Name the parasite shown.
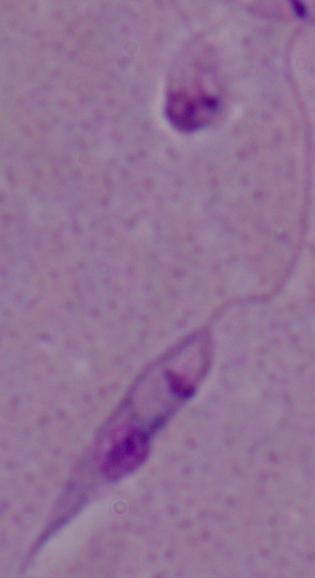
Leishmania.

Captured at 1000x magnification. Photomicrograph.